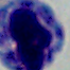
1000x magnification. Micrograph. A white blood cell is shown.